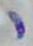 Toxoplasma gondii is seen. Micrograph. Captured at 1000x magnification.